State which parasite is depicted.
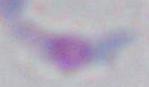
Toxoplasma gondii.

{
  "magnification": "1000x",
  "modality": "micrograph"
}